State which cell type is depicted.
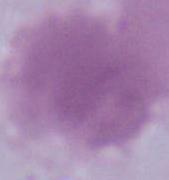

An erythrocyte.

Summary:
  - Modality: photomicrograph
  - Magnification: 1000x